State the blood parasite species.
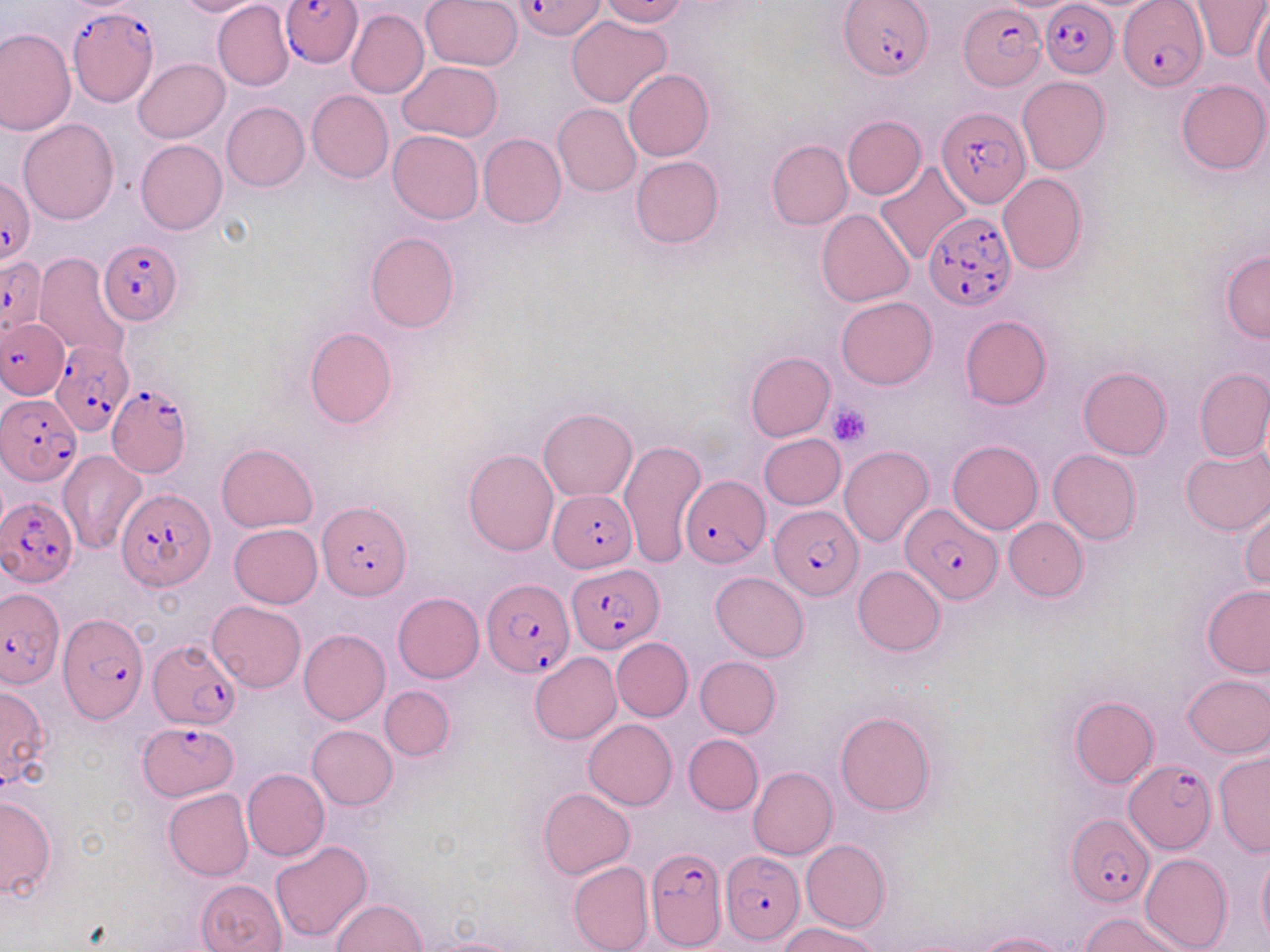
Plasmodium falciparum.

Summary:
  - Coordinate format: approximate bounding boxes as named x1/y1/x2/y2 corners in pixels
  - Uninfected red blood cell locations: (x1=173, y1=0, x2=265, y2=16), (x1=212, y1=0, x2=293, y2=91), (x1=421, y1=0, x2=522, y2=71), (x1=597, y1=0, x2=689, y2=26), (x1=1190, y1=1, x2=1268, y2=61), (x1=1232, y1=3, x2=1268, y2=84), (x1=1252, y1=6, x2=1270, y2=96), (x1=346, y1=8, x2=429, y2=98), (x1=566, y1=16, x2=672, y2=107), (x1=0, y1=28, x2=75, y2=137), (x1=134, y1=58, x2=229, y2=143), (x1=397, y1=60, x2=503, y2=142), (x1=624, y1=69, x2=713, y2=161), (x1=1017, y1=77, x2=1110, y2=174), (x1=1175, y1=79, x2=1270, y2=175), (x1=307, y1=90, x2=393, y2=184), (x1=222, y1=102, x2=309, y2=192), (x1=553, y1=104, x2=641, y2=197), (x1=842, y1=115, x2=925, y2=199), (x1=19, y1=118, x2=118, y2=223), (x1=388, y1=130, x2=483, y2=224), (x1=479, y1=134, x2=567, y2=228), (x1=135, y1=139, x2=227, y2=235), (x1=766, y1=140, x2=853, y2=230), (x1=629, y1=156, x2=725, y2=249), (x1=874, y1=160, x2=973, y2=264), (x1=997, y1=174, x2=1086, y2=275), (x1=817, y1=209, x2=916, y2=308), (x1=365, y1=233, x2=459, y2=332), (x1=35, y1=250, x2=130, y2=359), (x1=1220, y1=250, x2=1270, y2=342), (x1=835, y1=297, x2=936, y2=390), (x1=959, y1=316, x2=1050, y2=410), (x1=304, y1=327, x2=397, y2=428), (x1=745, y1=350, x2=835, y2=441), (x1=1077, y1=366, x2=1171, y2=459), (x1=1195, y1=370, x2=1270, y2=462), (x1=538, y1=408, x2=637, y2=501), (x1=758, y1=434, x2=845, y2=510), (x1=618, y1=439, x2=704, y2=568), (x1=947, y1=439, x2=1043, y2=534), (x1=216, y1=443, x2=317, y2=532), (x1=838, y1=446, x2=933, y2=547), (x1=1180, y1=446, x2=1270, y2=535), (x1=463, y1=449, x2=559, y2=556), (x1=1048, y1=449, x2=1141, y2=545), (x1=57, y1=450, x2=147, y2=555), (x1=1239, y1=502, x2=1269, y2=592), (x1=1003, y1=517, x2=1088, y2=601), (x1=229, y1=524, x2=322, y2=608), (x1=853, y1=564, x2=946, y2=655), (x1=710, y1=571, x2=809, y2=661), (x1=1201, y1=585, x2=1270, y2=677), (x1=393, y1=593, x2=485, y2=683), (x1=209, y1=601, x2=305, y2=692), (x1=298, y1=629, x2=391, y2=725), (x1=611, y1=638, x2=694, y2=721), (x1=529, y1=653, x2=621, y2=744), (x1=694, y1=656, x2=781, y2=737), (x1=1183, y1=673, x2=1269, y2=758), (x1=0, y1=684, x2=52, y2=792), (x1=380, y1=685, x2=455, y2=761), (x1=1069, y1=696, x2=1158, y2=788), (x1=835, y1=710, x2=936, y2=816), (x1=584, y1=719, x2=677, y2=810), (x1=307, y1=725, x2=397, y2=810), (x1=683, y1=734, x2=763, y2=814), (x1=1214, y1=752, x2=1270, y2=858), (x1=748, y1=766, x2=837, y2=860), (x1=242, y1=768, x2=330, y2=860), (x1=538, y1=787, x2=634, y2=879), (x1=163, y1=789, x2=254, y2=881), (x1=0, y1=796, x2=57, y2=900), (x1=801, y1=839, x2=889, y2=932), (x1=271, y1=841, x2=372, y2=943), (x1=1256, y1=847, x2=1269, y2=948), (x1=1141, y1=853, x2=1232, y2=952), (x1=567, y1=861, x2=653, y2=952), (x1=197, y1=879, x2=287, y2=952), (x1=332, y1=898, x2=425, y2=951), (x1=1080, y1=911, x2=1187, y2=952), (x1=779, y1=922, x2=885, y2=952), (x1=973, y1=931, x2=1069, y2=952), (x1=419, y1=935, x2=523, y2=952)
  - Plasmodium falciparum-infected red blood cell locations: (x1=282, y1=0, x2=363, y2=68), (x1=518, y1=0, x2=606, y2=40), (x1=1041, y1=1, x2=1118, y2=78), (x1=1116, y1=1, x2=1208, y2=91), (x1=839, y1=3, x2=931, y2=79), (x1=960, y1=3, x2=1045, y2=92), (x1=68, y1=6, x2=158, y2=107), (x1=937, y1=105, x2=1031, y2=210), (x1=2, y1=175, x2=35, y2=263), (x1=922, y1=212, x2=1015, y2=311), (x1=99, y1=238, x2=183, y2=324), (x1=0, y1=257, x2=47, y2=334), (x1=1, y1=318, x2=67, y2=397), (x1=50, y1=340, x2=132, y2=436), (x1=107, y1=381, x2=193, y2=479), (x1=3, y1=393, x2=82, y2=483), (x1=680, y1=475, x2=769, y2=568), (x1=549, y1=487, x2=636, y2=571), (x1=118, y1=488, x2=214, y2=591), (x1=0, y1=498, x2=77, y2=590), (x1=317, y1=501, x2=412, y2=600), (x1=899, y1=501, x2=1001, y2=606), (x1=768, y1=505, x2=861, y2=600), (x1=566, y1=566, x2=662, y2=654), (x1=482, y1=577, x2=572, y2=678), (x1=1, y1=591, x2=63, y2=688), (x1=57, y1=613, x2=147, y2=725), (x1=148, y1=641, x2=241, y2=729), (x1=137, y1=720, x2=236, y2=798), (x1=1125, y1=760, x2=1216, y2=852), (x1=1066, y1=815, x2=1154, y2=908), (x1=645, y1=846, x2=726, y2=948), (x1=718, y1=849, x2=806, y2=945)
  - Platelet locations: (x1=827, y1=404, x2=872, y2=447)
  - Preparation: thin blood smear
  - Modality: optical microscopy
  - Field of view: single
  - Stain: May-Grünwald-Giemsa
  - Magnification: 1000x
  - Image size: 1270×952 pixels